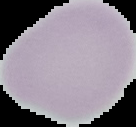

malaria status = uninfected
preparation = thin blood film
image type = segmented cell region with the area outside set to black
image size = 136×127 pixels